Report the malaria status of this cell.
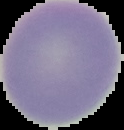

Uninfected.

Summary:
  - Image size: 124×130 pixels
  - Image type: cell region segmented out of the field of view; surrounding area masked to black
  - Preparation: thin blood smear